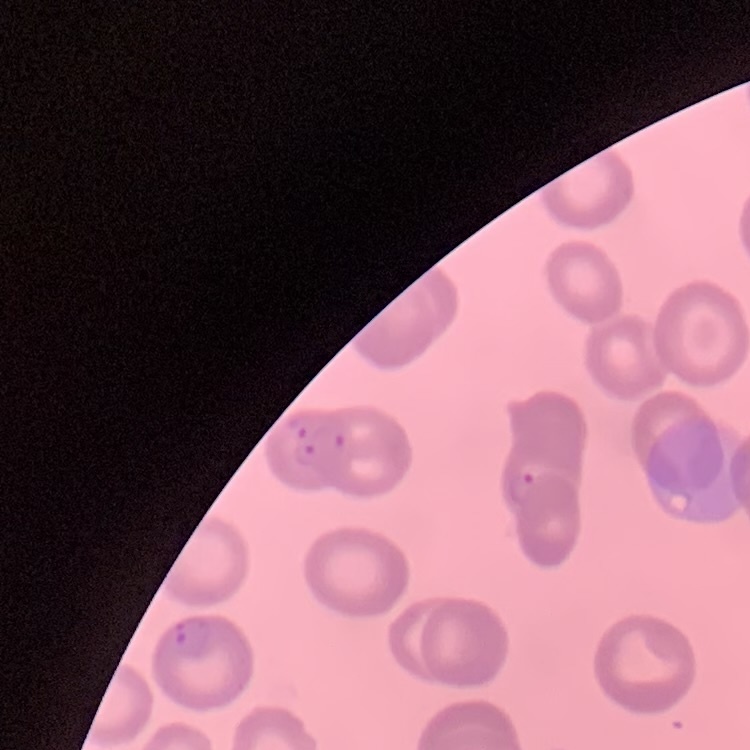

red blood cell morphology = no rouleaux formation
stain = Field's or Giemsa
preparation = thin blood smear
image type = square crop of a larger photomicrograph